Assess the morphology of the erythrocytes.
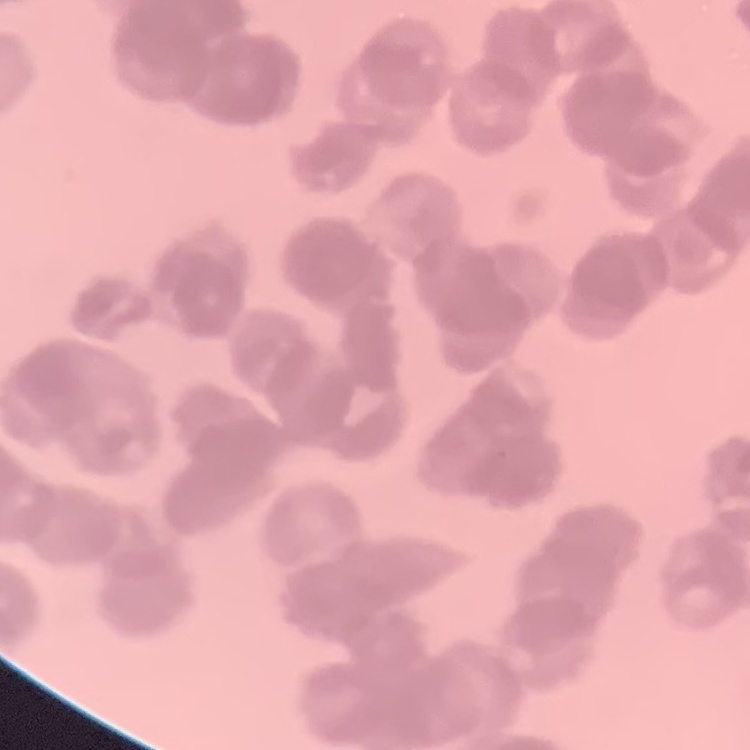

They show rouleaux formation.

Summary:
  - Stain: Field's or Giemsa
  - Preparation: thin peripheral smear
  - Image type: one tile cut from a larger photomicrograph